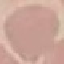 Result: negative for malaria parasites. Thin smear of blood. Acquired by smartphone through the microscope eyepiece. Automatically extracted cell patch, resized to 64 × 64 pixels. Giemsa stain.